State the blood parasite species.
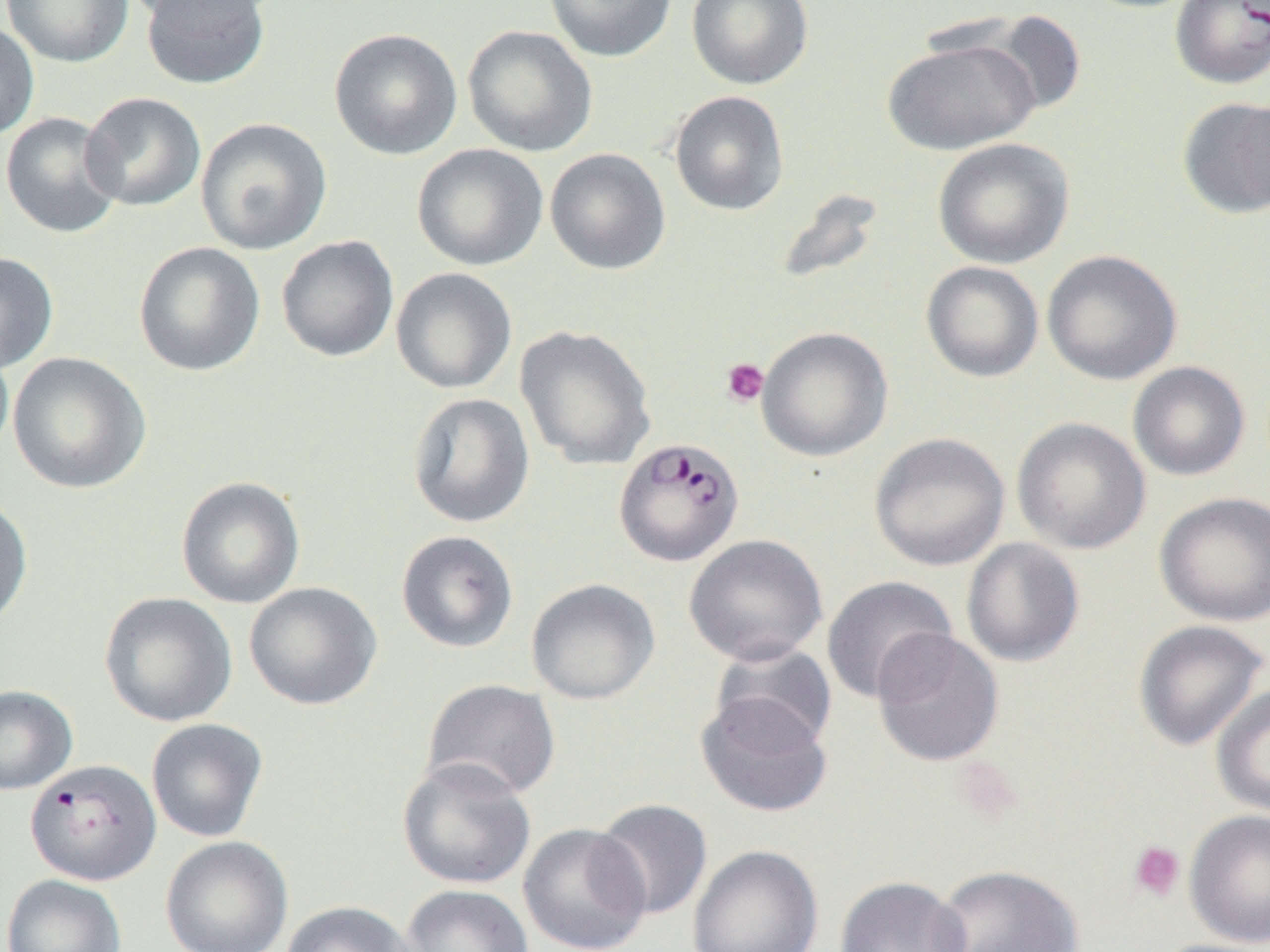
Plasmodium falciparum.

Summary:
  - Coordinate format: approximate bounding boxes as [x1, y1, x2, y2] in pixels
  - Uninfected red blood cell locations: [2, 0, 134, 68], [121, 0, 271, 25], [139, 0, 270, 90], [544, 0, 677, 62], [686, 0, 814, 90], [979, 9, 1088, 118], [0, 21, 40, 141], [462, 24, 598, 157], [329, 28, 462, 160], [882, 36, 1040, 155], [668, 90, 789, 216], [80, 91, 206, 211], [1176, 95, 1270, 218], [0, 111, 124, 239], [195, 117, 333, 255], [932, 137, 1075, 269], [411, 143, 548, 272], [545, 148, 670, 275], [772, 187, 886, 287], [276, 235, 399, 363], [133, 241, 266, 377], [1041, 250, 1183, 385], [0, 251, 59, 374], [921, 261, 1044, 382], [390, 267, 517, 394], [514, 325, 656, 470], [756, 326, 893, 462], [0, 341, 14, 465], [7, 351, 151, 494], [1127, 361, 1250, 481], [406, 392, 535, 528], [1011, 417, 1151, 555], [869, 432, 1010, 571], [175, 475, 306, 609], [1153, 491, 1270, 628], [0, 493, 33, 631], [396, 530, 519, 653], [684, 534, 828, 666], [961, 538, 1085, 667], [821, 576, 957, 704], [526, 578, 661, 704], [244, 581, 382, 710], [99, 592, 238, 727], [1132, 619, 1269, 751], [871, 628, 1004, 767], [709, 642, 838, 752], [421, 678, 561, 801], [1211, 684, 1270, 819], [0, 685, 78, 795], [695, 692, 834, 818], [145, 718, 269, 842], [396, 756, 536, 890], [593, 798, 713, 921], [1184, 809, 1270, 947], [518, 823, 652, 952], [160, 835, 293, 952], [687, 844, 824, 952], [933, 863, 1084, 952], [1, 873, 127, 952], [834, 875, 970, 952], [400, 884, 535, 952], [281, 901, 417, 952], [1149, 938, 1270, 952]
  - Plasmodium falciparum-infected red blood cell locations: [1169, 0, 1270, 90], [613, 437, 745, 567], [25, 758, 161, 886]
  - Platelet locations: [721, 358, 769, 407], [1127, 840, 1186, 902]
  - Modality: light microscopy
  - Image size: 1270×952 pixels
  - Magnification: 1000x
  - Preparation: thin blood smear
  - Field of view: single